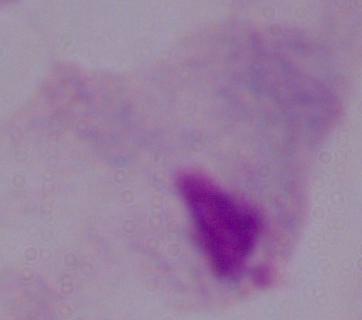
identification = trichomonad
modality = micrograph
magnification = 1000x